Identify the cell.
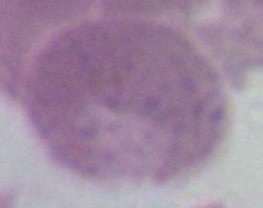

An erythrocyte.

modality = micrograph
magnification = 1000x